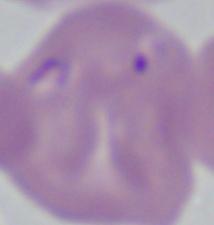

identification: Babesia
magnification: 1000x
modality: micrograph